Point out each Plasmodium parasite.
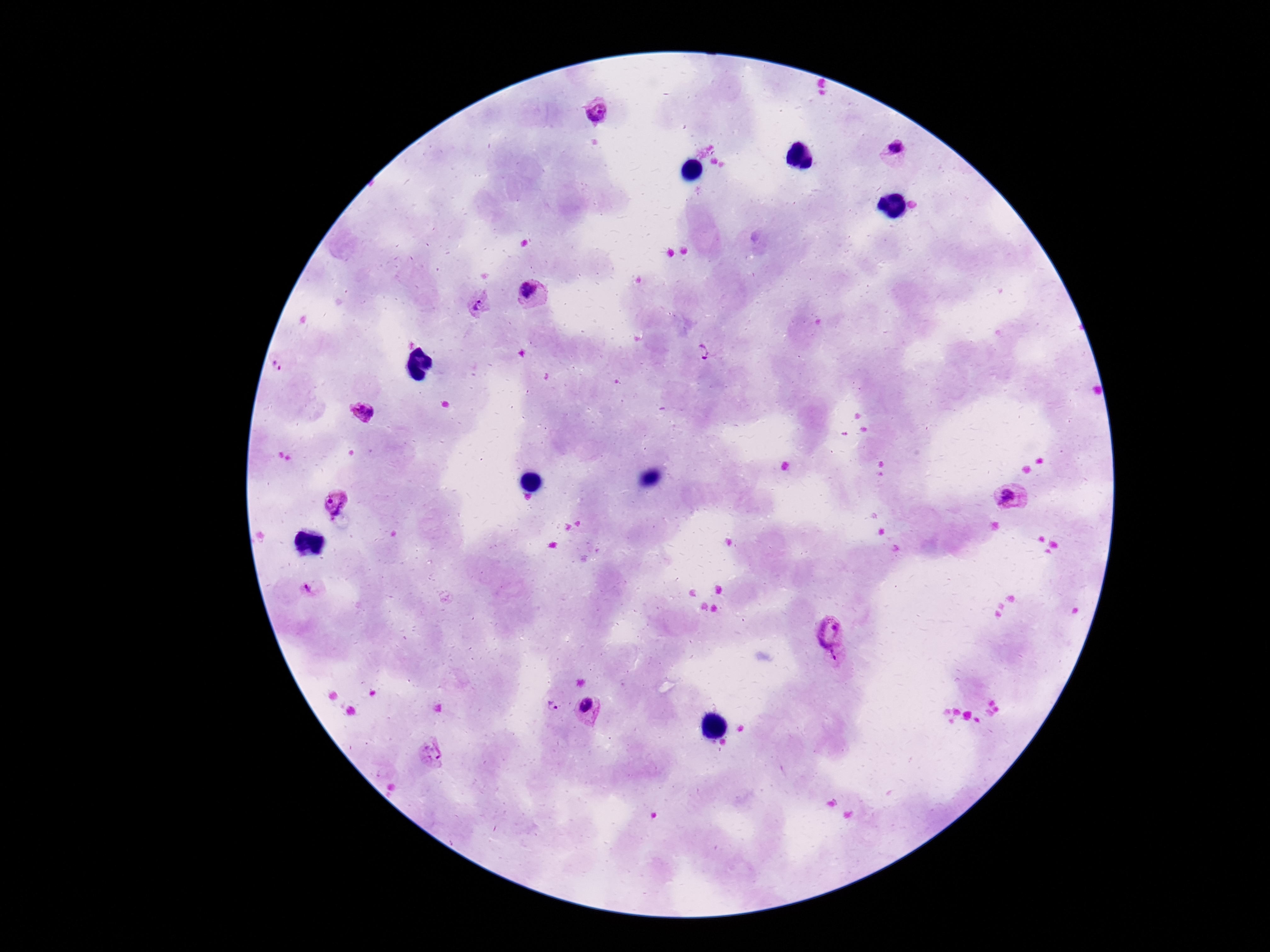

Approximate centers as {x, y} in pixels.
Plasmodium parasites: {597, 108}, {898, 153}, {532, 292}, {480, 305}, {703, 353}, {282, 363}, {363, 411}, {1012, 497}, {336, 501}, {311, 589}, {829, 628}, {837, 662}, {553, 706}, {590, 711}, {432, 756}.

Image is 1270×952 pixels. Single field of view. Patient malaria status: positive. Thick peripheral-blood smear. 100x magnification. Photographed through the microscope eyepiece with a smartphone camera. Giemsa-stained preparation.